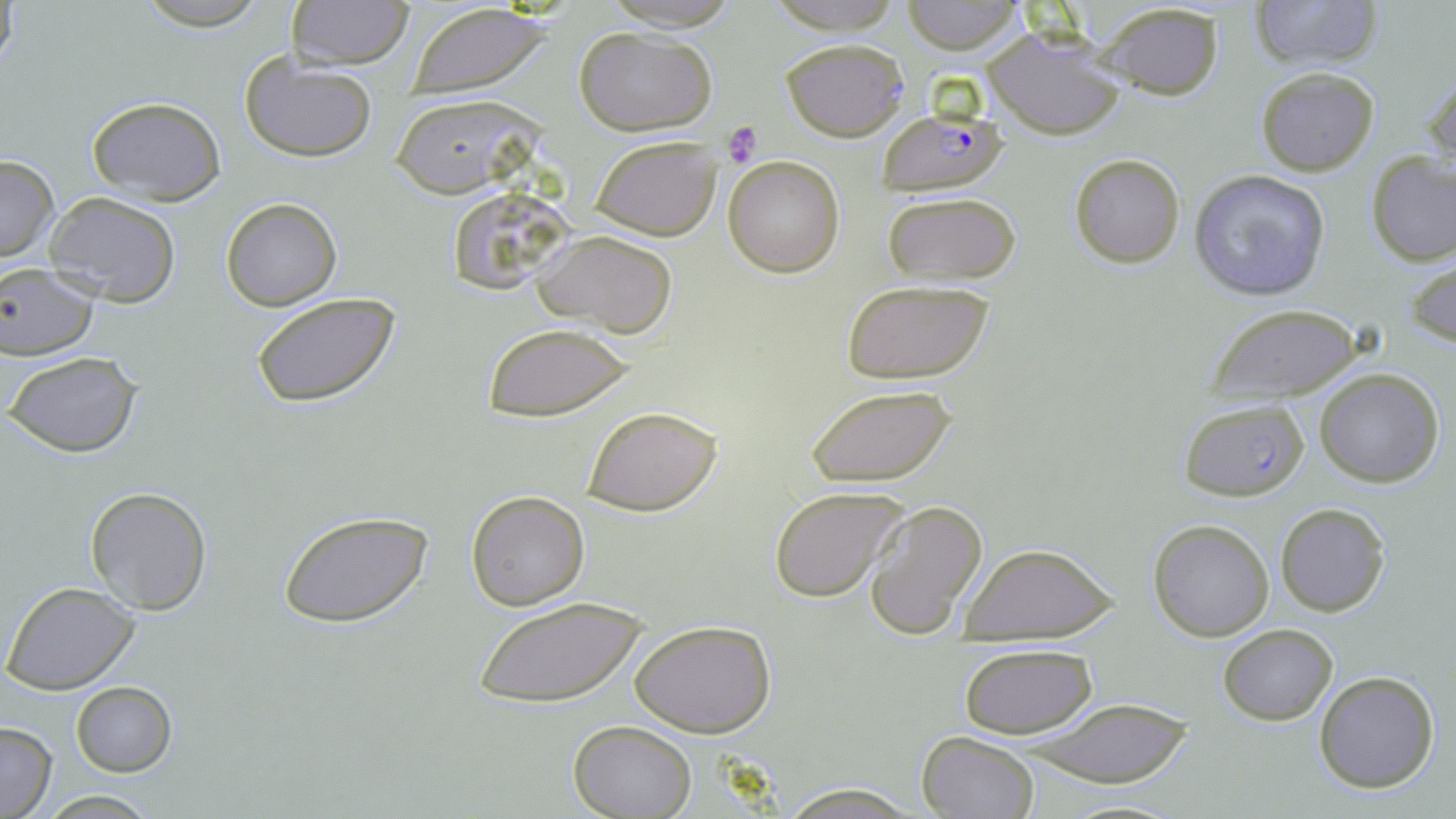
Summary:
  - Coordinate format: approximate bounding boxes as [x1, y1, x2, y2] in pixels
  - Uninfected red blood cell locations: [286, 0, 414, 70], [598, 0, 746, 31], [762, 0, 906, 32], [900, 0, 1025, 54], [1248, 0, 1385, 71], [1, 1, 24, 80], [405, 2, 558, 98], [1097, 2, 1225, 100], [129, 3, 275, 30], [984, 25, 1125, 140], [572, 26, 717, 133], [781, 38, 909, 141], [239, 52, 379, 164], [1254, 66, 1380, 176], [1422, 67, 1456, 181], [389, 93, 541, 198], [84, 95, 228, 203], [591, 134, 722, 240], [1365, 150, 1456, 266], [1068, 153, 1186, 269], [1, 155, 58, 264], [724, 155, 846, 276], [1188, 167, 1333, 303], [882, 190, 1022, 287], [45, 193, 181, 308], [221, 198, 342, 311], [534, 228, 678, 338], [1408, 257, 1456, 349], [0, 263, 101, 360], [842, 279, 992, 384], [250, 290, 403, 410], [1206, 304, 1364, 401], [480, 323, 635, 421], [5, 351, 142, 458], [1313, 368, 1444, 488], [804, 383, 956, 489], [581, 404, 722, 516], [768, 485, 911, 603], [84, 486, 213, 615], [465, 490, 590, 610], [863, 499, 989, 640], [1275, 503, 1390, 616], [279, 507, 434, 630], [1148, 518, 1274, 641], [959, 541, 1120, 643], [3, 581, 141, 695], [469, 600, 649, 708], [630, 618, 776, 738], [1219, 623, 1337, 726], [959, 643, 1097, 739], [1313, 671, 1440, 793], [71, 682, 175, 777], [1018, 695, 1201, 787], [569, 720, 696, 818], [0, 721, 56, 819], [914, 731, 1041, 819], [774, 784, 922, 817], [37, 792, 164, 818], [1051, 798, 1192, 819]
  - Plasmodium falciparum-infected red blood cell locations: [877, 106, 1006, 194], [1179, 398, 1310, 501]
  - Platelet locations: [721, 120, 764, 169]
  - Slide-level diagnosis: Plasmodium falciparum
  - Magnification: 1000x
  - Image size: 1456×819 pixels
  - Modality: light microscopy
  - Preparation: thin blood film
  - Field of view: single
  - Stain: May-Grünwald-Giemsa